Classify this cell by malaria status.
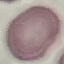
It is uninfected.

Summary:
  - Preparation: thin smear
  - Image type: cell patch, automatically extracted from a larger field of view and resized to 64 × 64 pixels
  - Capture: smartphone camera at the microscope eyepiece
  - Stain: Giemsa